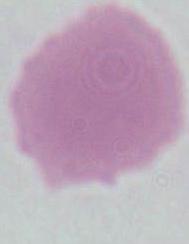
Summary:
  - Identification: erythrocyte
  - Magnification: 1000x
  - Modality: micrograph